Point out each Plasmodium parasite.
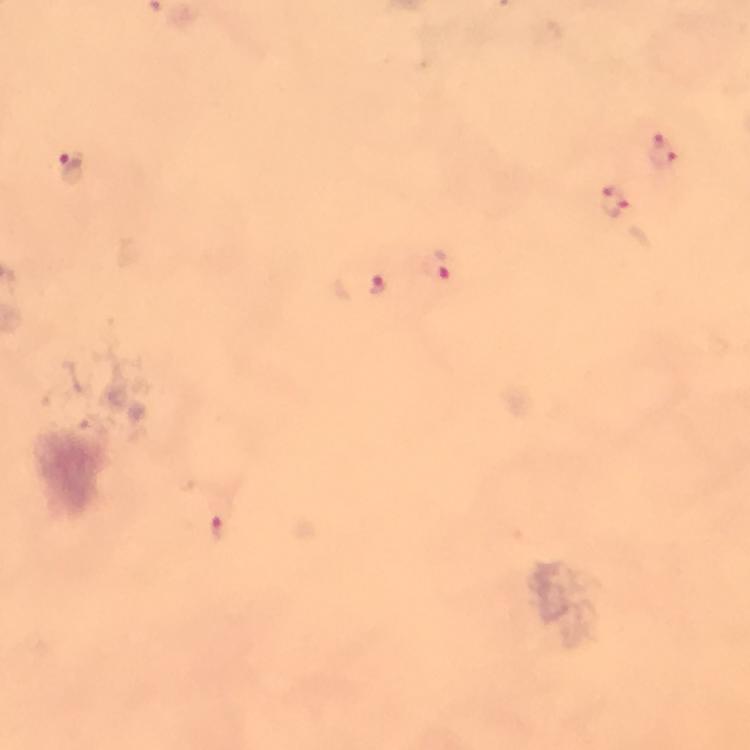
Approximate object centers, in pixels from the top-left corner.
Plasmodium parasites: (x=662, y=151), (x=73, y=169), (x=615, y=202), (x=437, y=265), (x=378, y=284), (x=219, y=526).

{
  "preparation": "thick smear",
  "capture": "smartphone photograph through a microscope",
  "stain": "Giemsa",
  "cropped_from": "a single field of view",
  "immersion_oil": "used",
  "magnification": "100x",
  "context": "from a diagnostic examination for malaria",
  "image_size": "750×750 pixels"
}